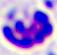

Summary:
  - Identification: leukocyte
  - Modality: photomicrograph
  - Magnification: 400x